Assess this cell for malaria.
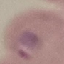
It is parasitized.

Summary:
  - Preparation: thin blood smear
  - Image type: automatically extracted cell patch, resized to 64 × 64 pixels
  - Stain: Giemsa
  - Capture: smartphone through the microscope eyepiece